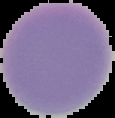 Image is 115×118 pixels. The area outside the segmented cell region is set to black. From a thin blood smear. Result: no Plasmodium parasites seen.